State which parasite is depicted.
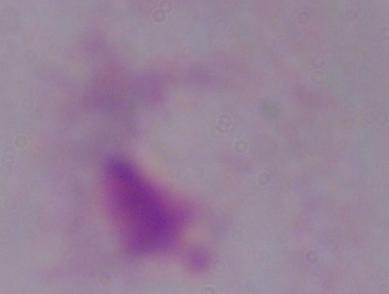

This is a trichomonad.

1000x magnification. Micrograph.